Outline platelets.
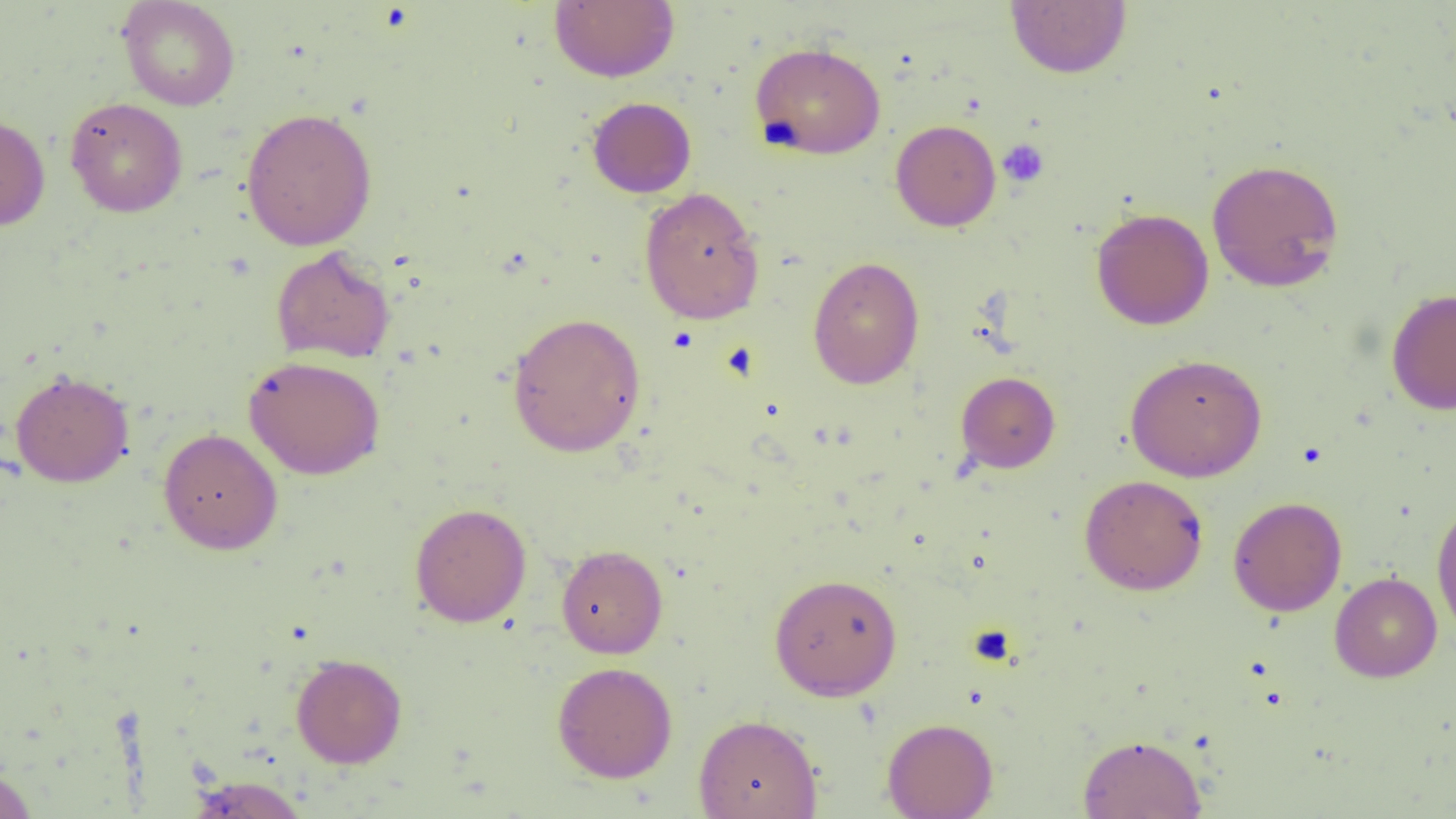

Approximate bounding boxes as (x1, y1, x2, y2) in pixels.
Platelets: (998, 139, 1050, 188).

Summary:
  - Uninfected red blood cell locations: (549, 0, 680, 83), (117, 1, 240, 111), (1005, 1, 1132, 79), (749, 41, 887, 159), (64, 97, 188, 217), (586, 97, 697, 198), (240, 107, 377, 251), (0, 113, 50, 231), (890, 119, 1002, 232), (1206, 158, 1345, 293), (639, 187, 765, 325), (1091, 208, 1214, 330), (271, 246, 396, 364), (807, 257, 925, 389), (1387, 288, 1456, 415), (507, 312, 646, 458), (1125, 353, 1267, 482), (244, 355, 385, 479), (10, 370, 134, 487), (956, 371, 1060, 473), (158, 427, 283, 555), (1079, 475, 1209, 596), (1228, 496, 1347, 616), (1431, 499, 1456, 641), (410, 502, 531, 628), (556, 544, 668, 658), (769, 572, 903, 701), (1330, 572, 1442, 682), (291, 653, 408, 768), (552, 661, 678, 783), (693, 713, 823, 819), (882, 717, 998, 819), (1077, 734, 1207, 818), (0, 764, 38, 819), (185, 775, 310, 818)
  - Slide-level diagnosis: negative for blood parasites
  - Magnification: 1000x
  - Preparation: thin blood film
  - Image size: 1456×819 pixels
  - Field of view: single
  - Modality: optical microscopy